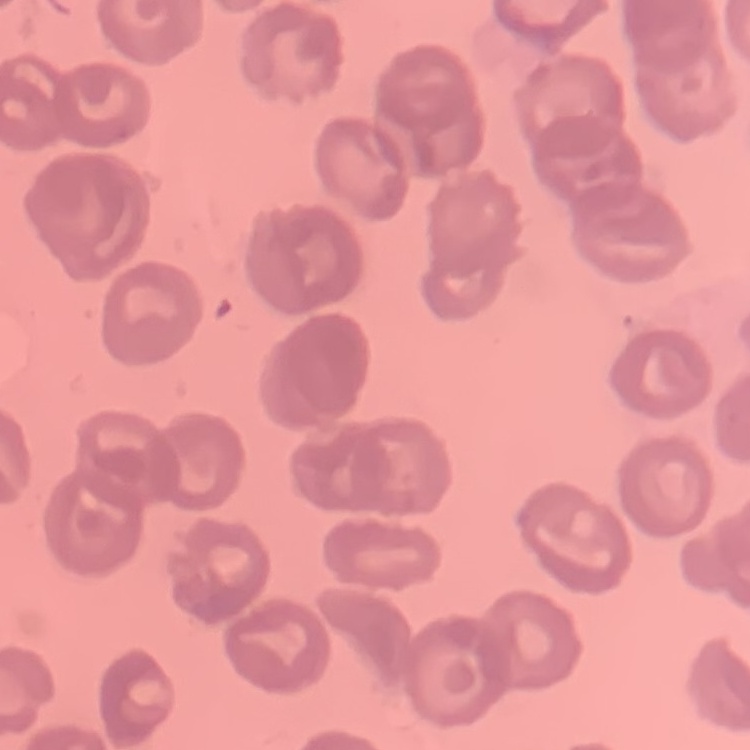

red blood cell morphology = no rouleaux formation
image type = one tile cut from a larger photomicrograph
preparation = thin blood film
stain = Field's or Giemsa